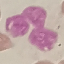
result = no malaria parasites seen
preparation = thin blood film
capture = smartphone through the microscope eyepiece
image type = automatically extracted cell patch, resized to 64 × 64 pixels
stain = Giemsa